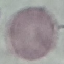

Result: negative for malaria parasites. Thin blood smear. Giemsa-stained preparation. Photographed with a smartphone camera at the microscope eyepiece. Cell patch, automatically extracted from a larger field of view and resized to 64 × 64 pixels.